Locate every leukocyte (white blood cell).
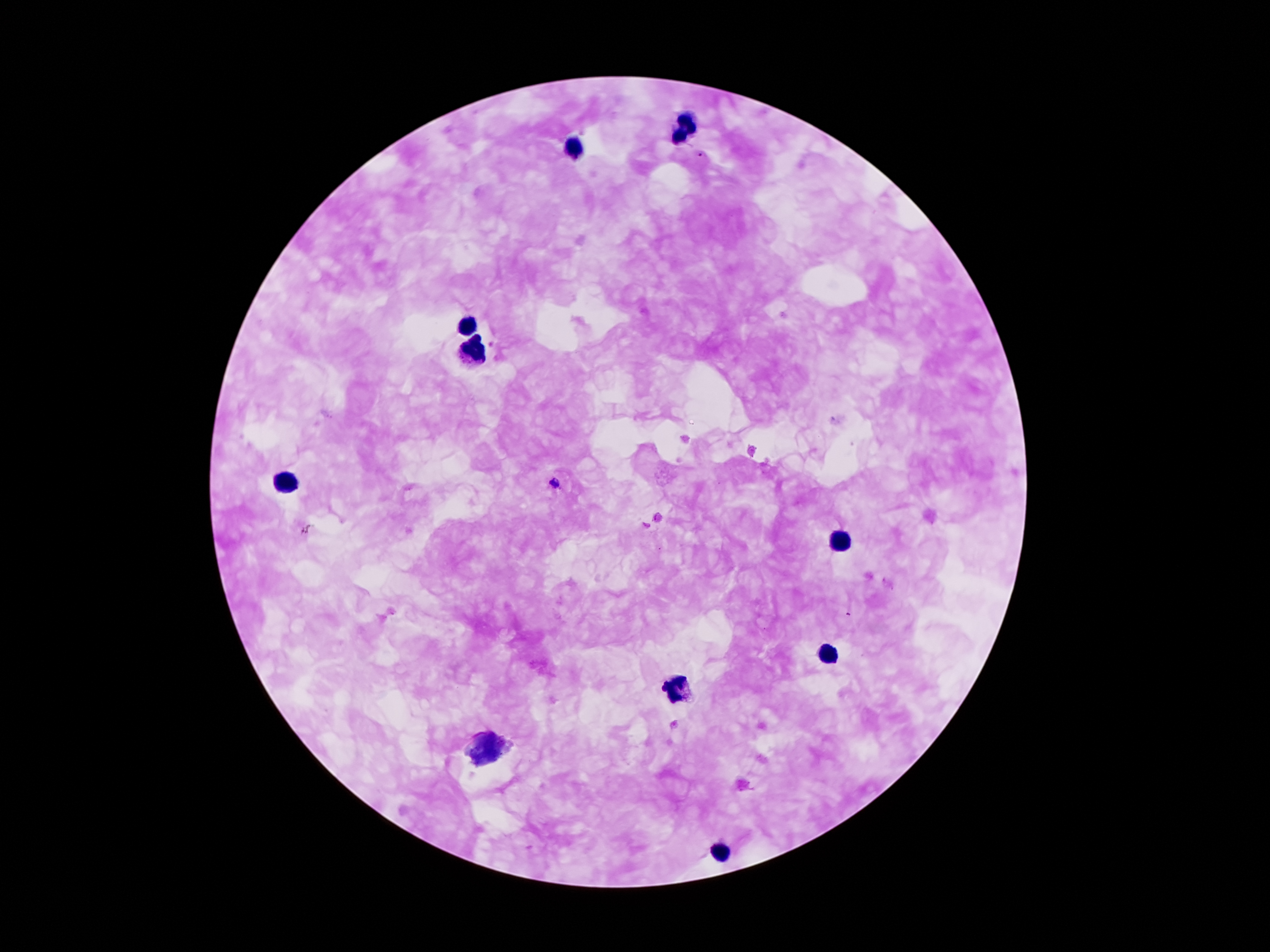

Approximate centers as {x, y} in pixels.
Leukocytes: {685, 129}, {570, 149}, {468, 328}, {475, 351}, {285, 484}, {842, 540}, {830, 658}, {676, 689}, {485, 752}, {719, 854}.

malaria parasite locations = {700, 155}, {554, 483}
capture = smartphone camera through the microscope eyepiece
magnification = 100x
preparation = thick blood smear
stain = Giemsa
patient malaria status = infected with Plasmodium falciparum
image size = 1270×952 pixels
field of view = single